Assess the morphology of the red blood cells.
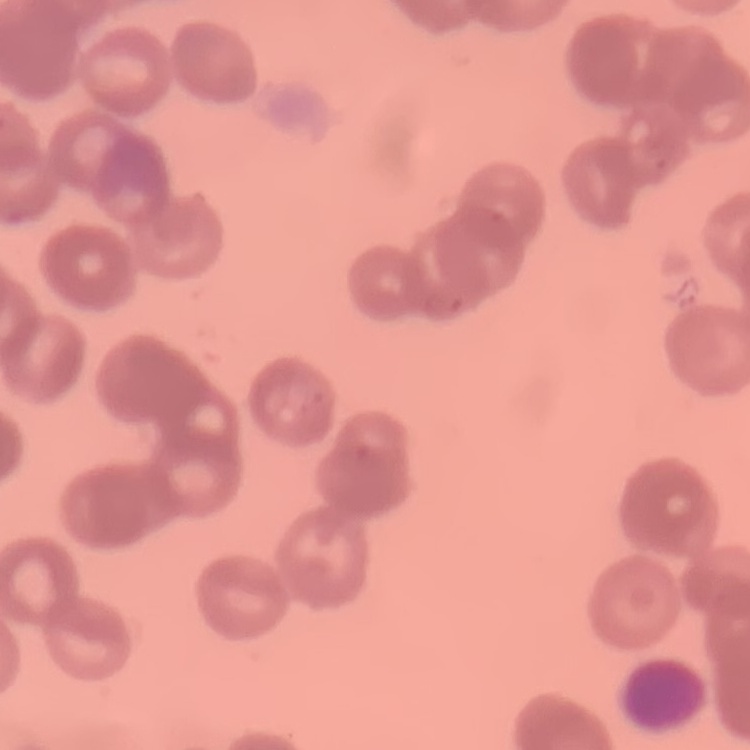

Rouleaux formation.

Field's or Giemsa stain. One tile cut from a larger photomicrograph. Thin blood film.